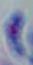
Toxoplasma gondii is shown. 1000x magnification. Micrograph.